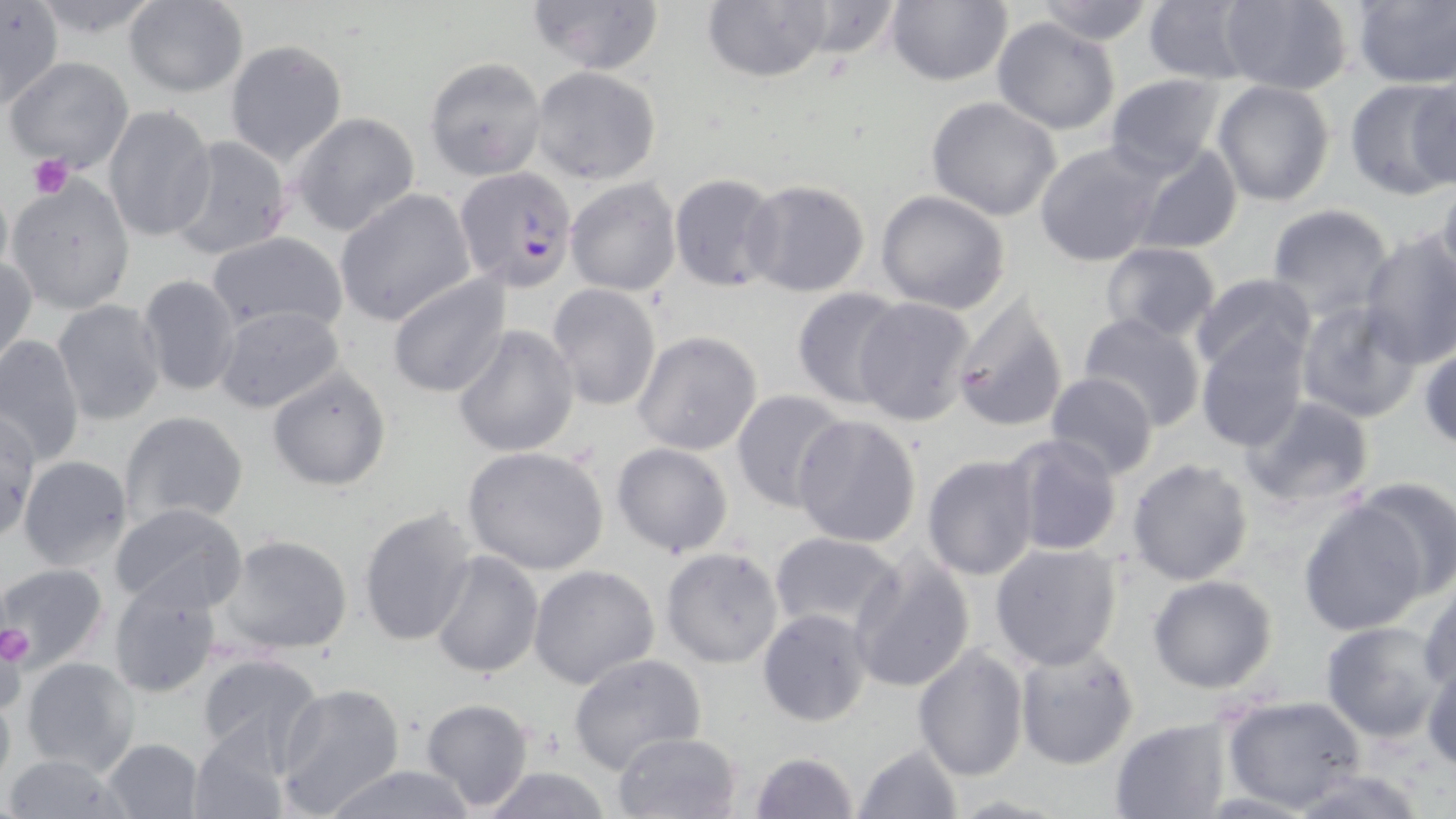

slide-level diagnosis = Plasmodium falciparum
image size = 1456×819 pixels
preparation = thin blood film
magnification = 1000x
uninfected red blood cell locations = approximate bounding boxes as [x1, y1, x2, y2] in pixels: [0, 0, 65, 109], [526, 0, 665, 77], [701, 0, 834, 84], [790, 0, 908, 59], [885, 0, 1012, 87], [1031, 0, 1158, 46], [1143, 0, 1257, 84], [1216, 0, 1355, 94], [122, 1, 249, 98], [1350, 2, 1456, 87], [991, 17, 1121, 135], [224, 40, 347, 168], [5, 55, 134, 173], [424, 56, 547, 179], [529, 66, 662, 186], [1103, 74, 1229, 179], [1404, 75, 1456, 194], [1346, 78, 1449, 201], [1212, 80, 1336, 206], [925, 96, 1063, 222], [103, 105, 216, 242], [290, 112, 422, 236], [166, 136, 294, 262], [1034, 142, 1165, 267], [1134, 144, 1244, 256], [669, 174, 784, 293], [7, 176, 137, 314], [0, 177, 13, 287], [566, 177, 681, 295], [744, 179, 872, 298], [1433, 186, 1456, 299], [334, 187, 478, 325], [875, 190, 1011, 313], [1265, 203, 1396, 319], [205, 231, 349, 335], [1357, 232, 1456, 368], [1099, 241, 1221, 343], [1, 253, 37, 371], [385, 271, 511, 397], [136, 273, 243, 398], [1191, 273, 1314, 379], [546, 283, 662, 411], [792, 287, 907, 408], [853, 296, 980, 429], [948, 296, 1070, 434], [52, 299, 168, 426], [1296, 300, 1423, 421], [212, 305, 346, 414], [1077, 311, 1207, 434], [451, 324, 580, 457], [1195, 328, 1309, 451], [632, 330, 763, 457], [0, 334, 86, 468], [1420, 344, 1456, 451], [264, 365, 393, 493], [1045, 372, 1157, 481], [729, 389, 848, 511], [1238, 395, 1378, 514], [0, 407, 41, 544], [120, 410, 250, 528], [791, 413, 922, 547], [1006, 434, 1126, 559], [611, 442, 733, 558], [462, 446, 610, 576], [922, 453, 1039, 581], [16, 454, 134, 571], [1126, 457, 1254, 587], [1349, 474, 1456, 598], [1298, 499, 1428, 634], [108, 504, 249, 616], [357, 505, 479, 647], [769, 531, 907, 637], [216, 533, 354, 659], [989, 542, 1123, 670], [660, 546, 784, 669], [428, 550, 543, 680], [847, 550, 977, 695], [528, 562, 661, 689], [0, 563, 109, 674], [1148, 573, 1278, 694], [106, 574, 225, 698], [1418, 582, 1456, 695], [1387, 602, 1456, 728], [758, 609, 873, 727], [1320, 620, 1447, 743], [1014, 643, 1141, 769], [913, 645, 1029, 782], [194, 652, 329, 773], [568, 654, 707, 774], [19, 656, 140, 775], [1423, 656, 1456, 773], [272, 682, 407, 816], [0, 687, 15, 791], [1221, 694, 1367, 811], [417, 697, 536, 812], [1109, 716, 1235, 819], [186, 727, 289, 818], [611, 730, 742, 818], [101, 737, 206, 819], [852, 742, 963, 819], [748, 751, 861, 819], [0, 753, 136, 818], [318, 765, 481, 819], [481, 766, 614, 819], [1282, 766, 1435, 819], [946, 794, 1074, 818]
modality = light microscopy
platelet locations = approximate bounding boxes as [x1, y1, x2, y2] in pixels: [27, 153, 73, 199], [0, 622, 34, 670]
Plasmodium falciparum-infected red blood cell locations = approximate bounding boxes as [x1, y1, x2, y2] in pixels: [455, 165, 578, 289]
field of view = one of a larger specimen
stain = May-Grünwald-Giemsa